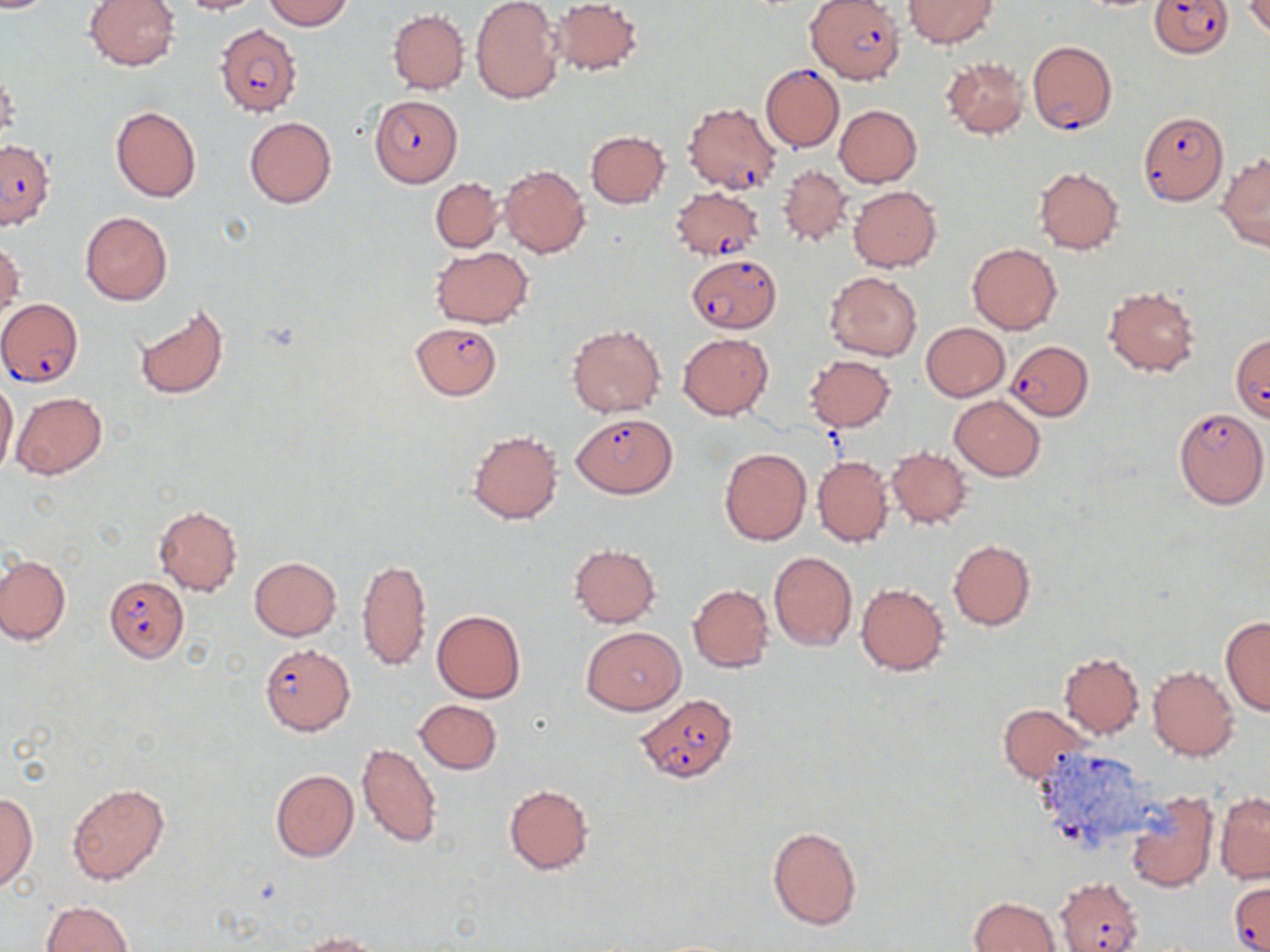

Summary:
  - Coordinate format: approximate bounding boxes as named x1/y1/x2/y2 corners in pixels
  - Uninfected red blood cell locations: (x1=0, y1=0, x2=59, y2=12), (x1=85, y1=0, x2=179, y2=71), (x1=172, y1=0, x2=263, y2=15), (x1=262, y1=0, x2=353, y2=30), (x1=471, y1=0, x2=563, y2=104), (x1=550, y1=0, x2=643, y2=75), (x1=903, y1=0, x2=999, y2=49), (x1=1243, y1=1, x2=1270, y2=37), (x1=387, y1=9, x2=468, y2=94), (x1=941, y1=56, x2=1029, y2=139), (x1=834, y1=105, x2=921, y2=187), (x1=110, y1=106, x2=201, y2=203), (x1=244, y1=116, x2=336, y2=209), (x1=585, y1=130, x2=671, y2=208), (x1=1218, y1=152, x2=1270, y2=250), (x1=777, y1=164, x2=852, y2=247), (x1=499, y1=165, x2=589, y2=258), (x1=1034, y1=167, x2=1124, y2=254), (x1=430, y1=177, x2=504, y2=252), (x1=849, y1=184, x2=942, y2=272), (x1=80, y1=210, x2=173, y2=305), (x1=1, y1=238, x2=23, y2=320), (x1=967, y1=243, x2=1062, y2=334), (x1=432, y1=247, x2=533, y2=327), (x1=824, y1=271, x2=922, y2=361), (x1=1103, y1=286, x2=1200, y2=376), (x1=134, y1=305, x2=230, y2=400), (x1=920, y1=322, x2=1009, y2=401), (x1=567, y1=324, x2=664, y2=416), (x1=678, y1=333, x2=773, y2=420), (x1=805, y1=355, x2=895, y2=431), (x1=0, y1=380, x2=18, y2=479), (x1=11, y1=392, x2=107, y2=479), (x1=949, y1=395, x2=1045, y2=481), (x1=468, y1=431, x2=562, y2=524), (x1=885, y1=446, x2=973, y2=528), (x1=719, y1=448, x2=811, y2=545), (x1=813, y1=456, x2=893, y2=548), (x1=153, y1=505, x2=242, y2=596), (x1=946, y1=539, x2=1035, y2=630), (x1=569, y1=545, x2=661, y2=627), (x1=768, y1=551, x2=858, y2=651), (x1=1, y1=555, x2=71, y2=645), (x1=249, y1=557, x2=342, y2=641), (x1=357, y1=558, x2=433, y2=671), (x1=855, y1=582, x2=950, y2=675), (x1=688, y1=584, x2=774, y2=673), (x1=433, y1=610, x2=526, y2=704), (x1=1220, y1=615, x2=1270, y2=716), (x1=580, y1=625, x2=686, y2=715), (x1=1058, y1=652, x2=1144, y2=738), (x1=1147, y1=664, x2=1240, y2=761), (x1=414, y1=700, x2=502, y2=774), (x1=997, y1=704, x2=1093, y2=785), (x1=357, y1=742, x2=441, y2=847), (x1=270, y1=769, x2=359, y2=862), (x1=66, y1=782, x2=169, y2=884), (x1=503, y1=784, x2=594, y2=875), (x1=1123, y1=789, x2=1218, y2=893), (x1=0, y1=791, x2=37, y2=894), (x1=1215, y1=791, x2=1269, y2=883), (x1=766, y1=824, x2=862, y2=931), (x1=968, y1=896, x2=1060, y2=952), (x1=42, y1=901, x2=133, y2=952), (x1=297, y1=931, x2=383, y2=952)
  - Plasmodium falciparum-infected red blood cell locations: (x1=1150, y1=0, x2=1233, y2=57), (x1=805, y1=1, x2=905, y2=83), (x1=215, y1=23, x2=302, y2=117), (x1=1027, y1=40, x2=1116, y2=134), (x1=759, y1=64, x2=844, y2=152), (x1=369, y1=95, x2=462, y2=186), (x1=682, y1=101, x2=782, y2=194), (x1=1137, y1=113, x2=1228, y2=204), (x1=0, y1=140, x2=53, y2=230), (x1=670, y1=186, x2=764, y2=260), (x1=686, y1=253, x2=782, y2=333), (x1=1, y1=298, x2=83, y2=388), (x1=411, y1=321, x2=502, y2=399), (x1=1230, y1=335, x2=1270, y2=421), (x1=1005, y1=340, x2=1094, y2=420), (x1=1173, y1=406, x2=1267, y2=509), (x1=572, y1=413, x2=676, y2=497), (x1=103, y1=577, x2=188, y2=661), (x1=259, y1=642, x2=355, y2=735), (x1=637, y1=693, x2=738, y2=783), (x1=1055, y1=877, x2=1143, y2=952), (x1=1228, y1=881, x2=1270, y2=952)
  - Slide-level diagnosis: Plasmodium falciparum
  - Preparation: thin blood smear
  - Image size: 1270×952 pixels
  - Stain: May-Grünwald-Giemsa
  - Magnification: 1000x
  - Modality: light microscopy
  - Field of view: single